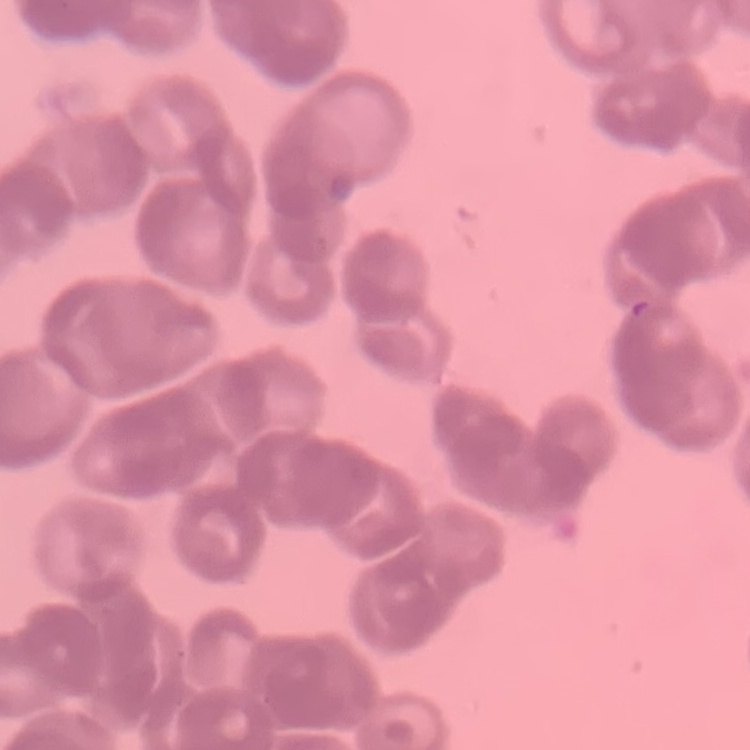

Summary:
  - Red blood cell morphology: rouleaux formation
  - Stain: Field's or Giemsa
  - Image type: square crop of a larger photomicrograph
  - Preparation: thin blood film